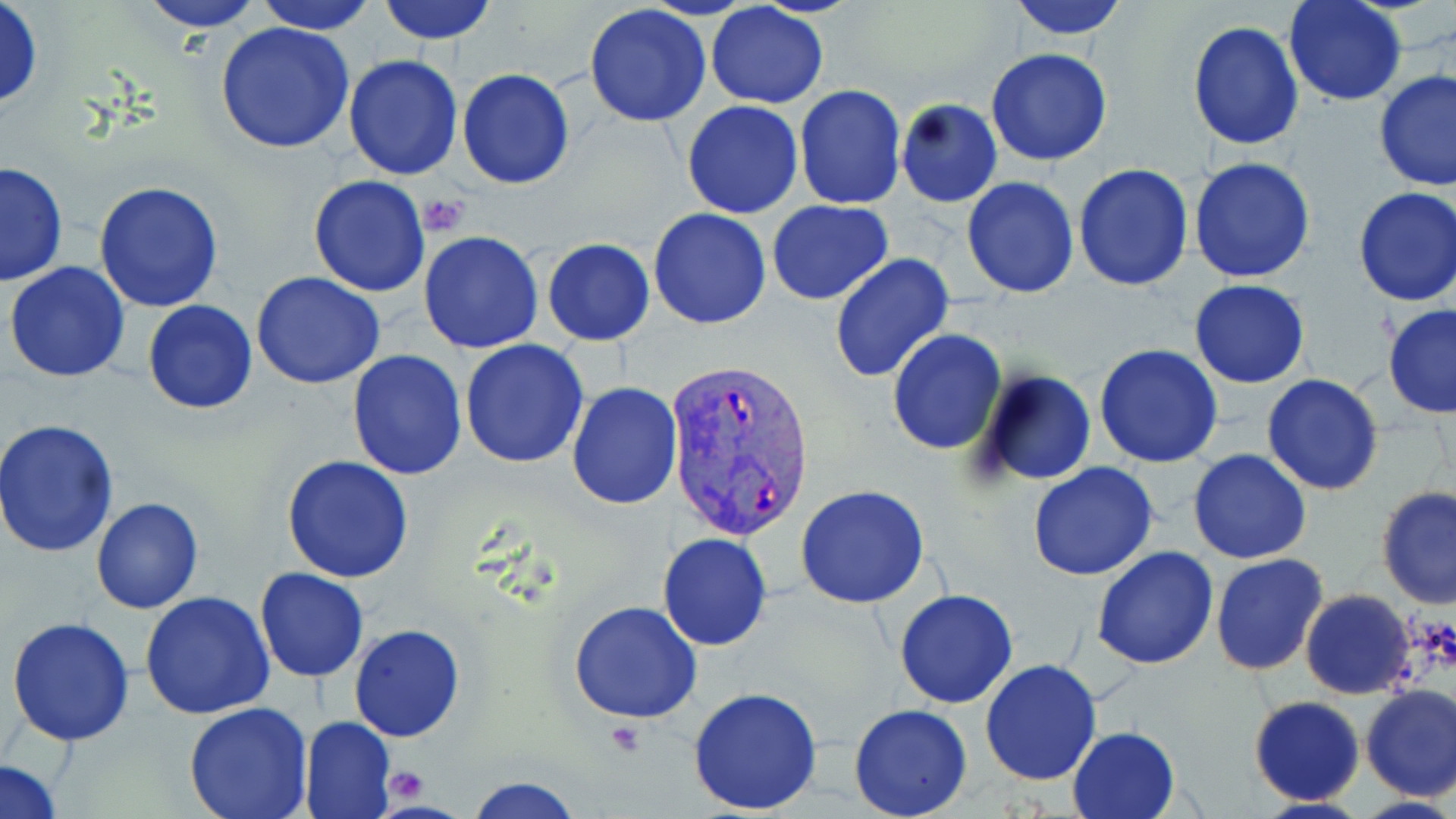

Approximate bounding boxes as (x1, y1, x2, y2) in pixels. Platelet locations: (419, 194, 469, 234), (385, 769, 428, 804). Uninfected red blood cell locations: (0, 0, 44, 110), (137, 0, 265, 31), (251, 0, 381, 34), (377, 0, 498, 44), (1011, 0, 1131, 41), (1283, 1, 1406, 105), (705, 3, 831, 108), (584, 5, 713, 128), (214, 20, 355, 156), (1187, 22, 1305, 151), (987, 48, 1113, 166), (342, 54, 462, 181), (457, 68, 575, 190), (1373, 69, 1456, 195), (794, 85, 906, 210), (895, 98, 1002, 208), (681, 100, 804, 219), (1188, 157, 1316, 284), (1, 160, 68, 285), (1073, 163, 1194, 290), (308, 174, 432, 296), (962, 177, 1079, 297), (94, 181, 224, 314), (1352, 186, 1456, 306), (768, 200, 894, 305), (648, 207, 774, 329), (419, 231, 543, 353), (542, 239, 655, 345), (829, 253, 955, 383), (5, 262, 131, 383), (251, 271, 386, 388), (1188, 279, 1310, 388), (143, 299, 258, 415), (1382, 305, 1456, 419), (886, 329, 1007, 455), (459, 339, 589, 468), (1094, 344, 1222, 467), (347, 351, 467, 481), (973, 370, 1097, 488), (1262, 374, 1383, 496), (567, 382, 683, 509), (1, 419, 120, 558), (1188, 449, 1312, 564), (281, 455, 414, 582), (1028, 462, 1160, 582), (796, 486, 931, 609), (1375, 486, 1456, 610), (90, 496, 203, 613), (657, 532, 772, 651), (1092, 546, 1219, 668), (1211, 554, 1329, 676), (254, 566, 369, 682), (894, 589, 1019, 709), (1300, 589, 1415, 699), (140, 593, 276, 719), (568, 600, 702, 723), (6, 616, 136, 746), (349, 624, 464, 742), (980, 659, 1104, 786), (1359, 685, 1456, 802), (687, 686, 823, 813), (1247, 696, 1364, 806), (182, 701, 314, 819), (848, 704, 974, 819), (300, 715, 396, 819), (1068, 726, 1181, 818), (1, 758, 64, 818), (464, 775, 583, 818). Plasmodium vivax-infected red blood cell locations: (666, 360, 815, 539). Slide-level diagnosis: Plasmodium vivax. Single field of view. Light microscopy. May-Grünwald-Giemsa-stained preparation. Image is 1456×819 pixels. 1000x magnification. Thin blood smear.